Outline each Plasmodium falciparum-infected red blood cell.
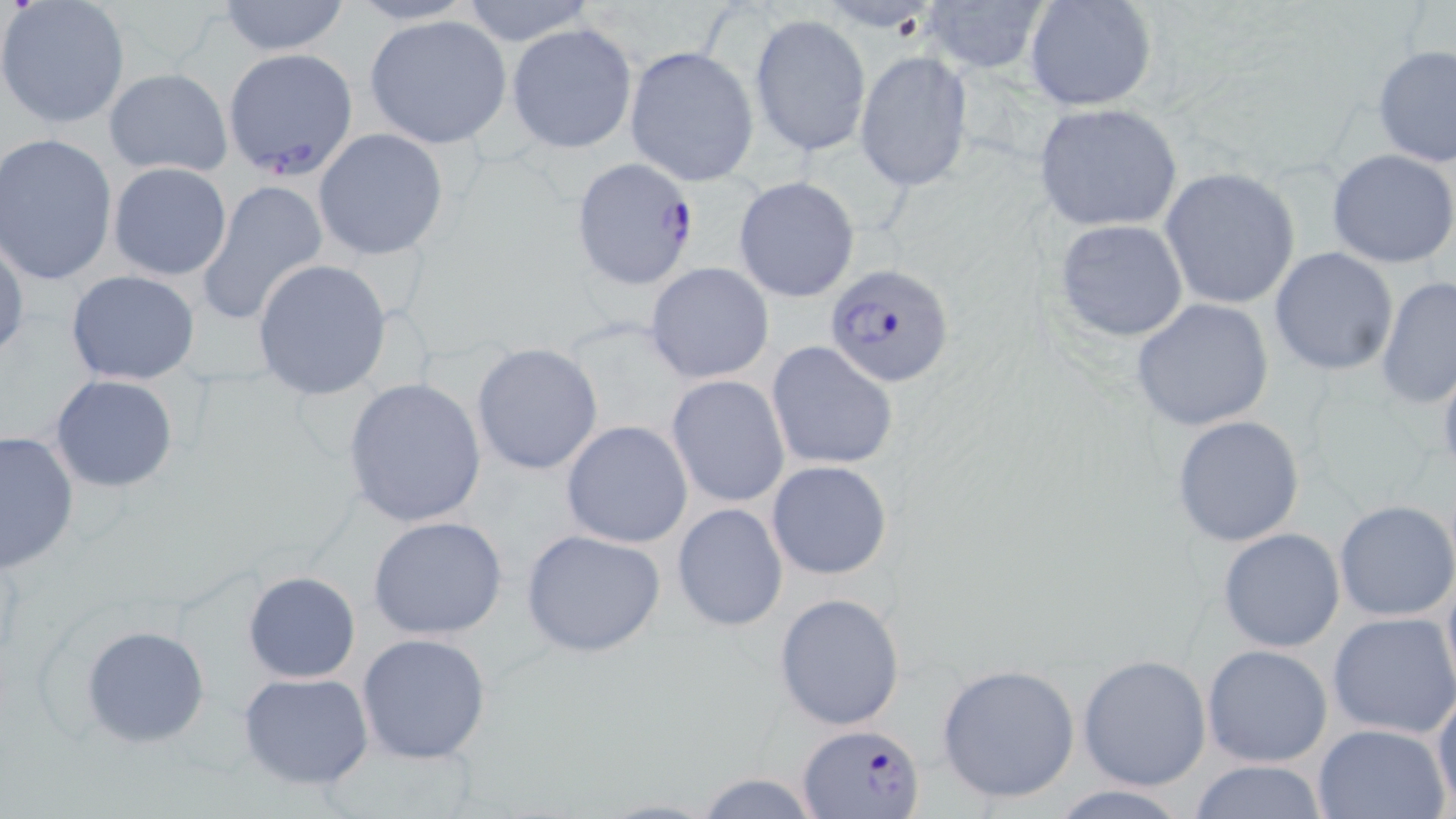
Approximate bounding boxes as [x1, y1, x2, y2] in pixels.
Plasmodium falciparum-infected red blood cells: [221, 48, 358, 178], [573, 158, 700, 290], [826, 266, 955, 386], [800, 721, 923, 818].

slide_level_diagnosis: Plasmodium falciparum
magnification: 1000x
uninfected_red_blood_cell_locations: 'approximate bounding boxes as [x1, y1, x2, y2] in pixels: [212, 0, 355, 56], [457, 0, 596, 48], [915, 0, 1051, 74], [1024, 0, 1158, 112], [1, 2, 132, 129], [749, 14, 871, 157], [364, 15, 513, 149], [506, 23, 637, 155], [624, 45, 760, 185], [1372, 45, 1456, 166], [854, 51, 972, 191], [103, 67, 232, 177], [1032, 102, 1183, 233], [314, 128, 449, 259], [1, 133, 119, 286], [1327, 149, 1456, 267], [107, 163, 233, 281], [1159, 167, 1301, 310], [732, 176, 861, 304], [196, 179, 327, 326], [1051, 218, 1191, 341], [0, 229, 28, 364], [1269, 247, 1398, 376], [251, 259, 393, 400], [645, 262, 776, 384], [64, 270, 201, 385], [1375, 275, 1456, 411], [1131, 298, 1277, 433], [766, 339, 898, 472], [470, 342, 604, 477], [48, 374, 181, 492], [666, 375, 790, 507], [341, 377, 487, 529], [1171, 414, 1305, 547], [560, 420, 694, 549], [1, 429, 79, 573], [766, 459, 892, 580], [1334, 499, 1456, 622], [670, 502, 789, 633], [367, 516, 511, 641], [520, 528, 667, 659], [1217, 528, 1347, 651], [1440, 564, 1455, 702], [243, 570, 362, 682], [773, 590, 905, 731], [1326, 612, 1456, 740], [79, 625, 212, 749], [357, 632, 492, 763], [1201, 644, 1333, 767], [1077, 654, 1212, 791], [934, 662, 1082, 804], [239, 672, 373, 790], [1431, 688, 1456, 810], [1312, 722, 1452, 819], [1186, 758, 1330, 819], [691, 770, 823, 818], [1046, 783, 1194, 817]'
modality: light microscopy
image_size: 1456×819 pixels
stain: May-Grünwald-Giemsa
field_of_view: one of a larger specimen
preparation: thin blood smear